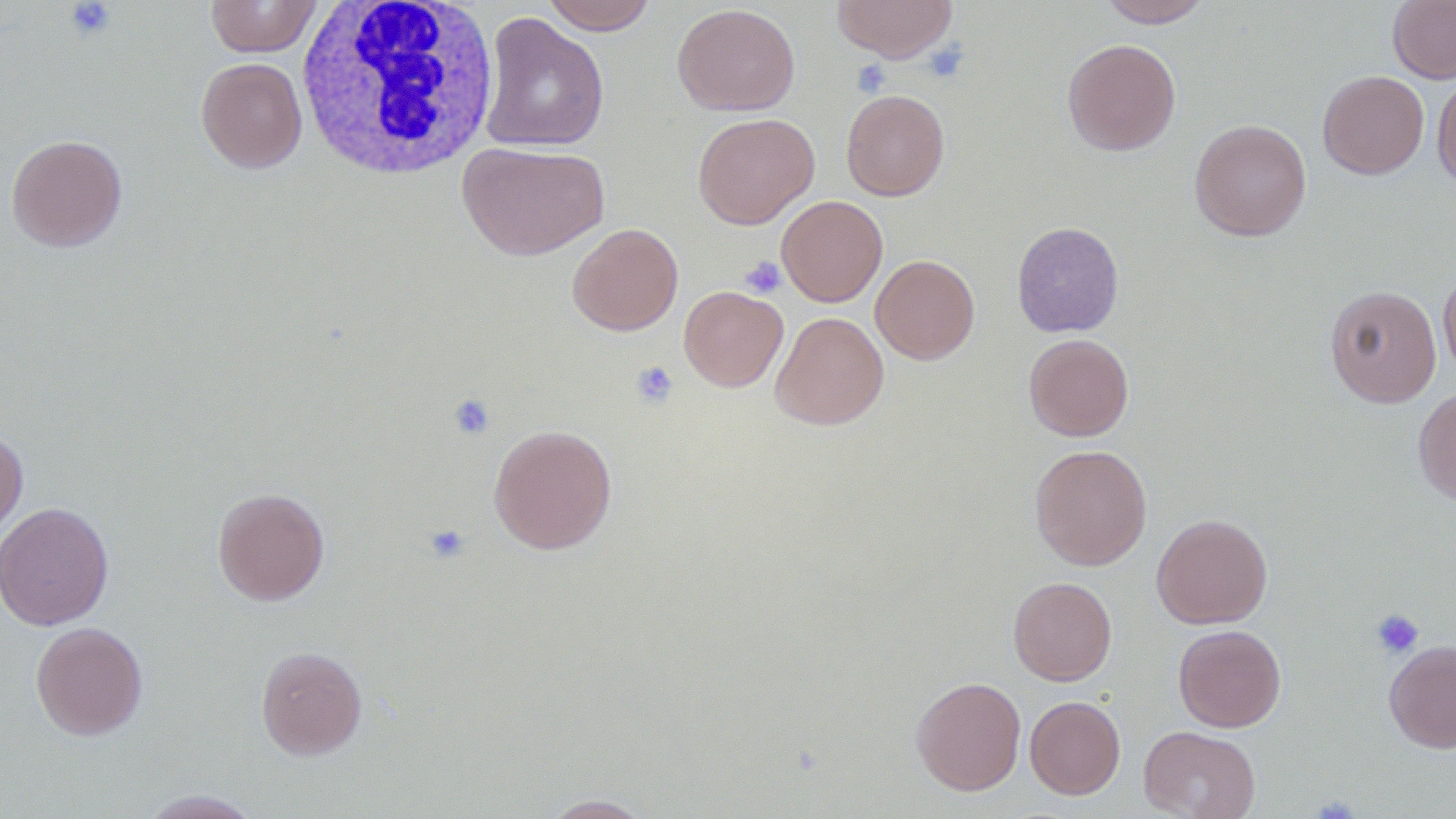
slide-level diagnosis = negative for blood parasites
preparation = thin blood film
image size = 1456×819 pixels
field of view = one of a larger specimen
platelet locations = approximate bounding boxes as (x1,y1)-(x2,y2) corner pairs in pixels: (65,0)-(116,41), (922,42)-(969,84), (852,59)-(891,97), (739,256)-(787,299), (630,360)-(679,409), (447,393)-(495,440), (423,524)-(470,563), (1370,609)-(1424,659)
white blood cell locations = approximate bounding boxes as (x1,y1)-(x2,y2) corner pairs in pixels: (295,0)-(501,181)
magnification = 1000x
uninfected red blood cell locations = approximate bounding boxes as (x1,y1)-(x2,y2) corner pairs in pixels: (205,0)-(323,57), (541,0)-(658,35), (831,0)-(959,63), (1097,0)-(1213,27), (1388,0)-(1456,84), (672,3)-(801,116), (479,12)-(610,153), (1062,39)-(1181,155), (196,57)-(307,173), (1317,70)-(1429,179), (1432,74)-(1456,192), (841,89)-(949,201), (692,111)-(819,229), (1189,119)-(1311,241), (6,134)-(128,252), (457,141)-(610,260), (777,195)-(888,307), (567,223)-(683,335), (1011,223)-(1124,337), (871,254)-(980,365), (1438,269)-(1456,380), (1324,285)-(1441,407), (678,286)-(788,392), (770,312)-(889,430), (1024,333)-(1134,441), (1413,387)-(1456,506), (488,424)-(618,554), (0,428)-(28,545), (1030,444)-(1152,570), (212,486)-(330,605), (0,502)-(113,631), (1152,514)-(1273,628), (1008,577)-(1116,686), (30,622)-(148,740), (1173,624)-(1287,732), (1384,640)-(1456,754), (255,646)-(368,759), (911,676)-(1026,796), (1025,695)-(1125,799), (1139,725)-(1260,819), (137,789)-(264,818), (539,793)-(655,818)
modality = optical microscopy